Name the blood parasite species.
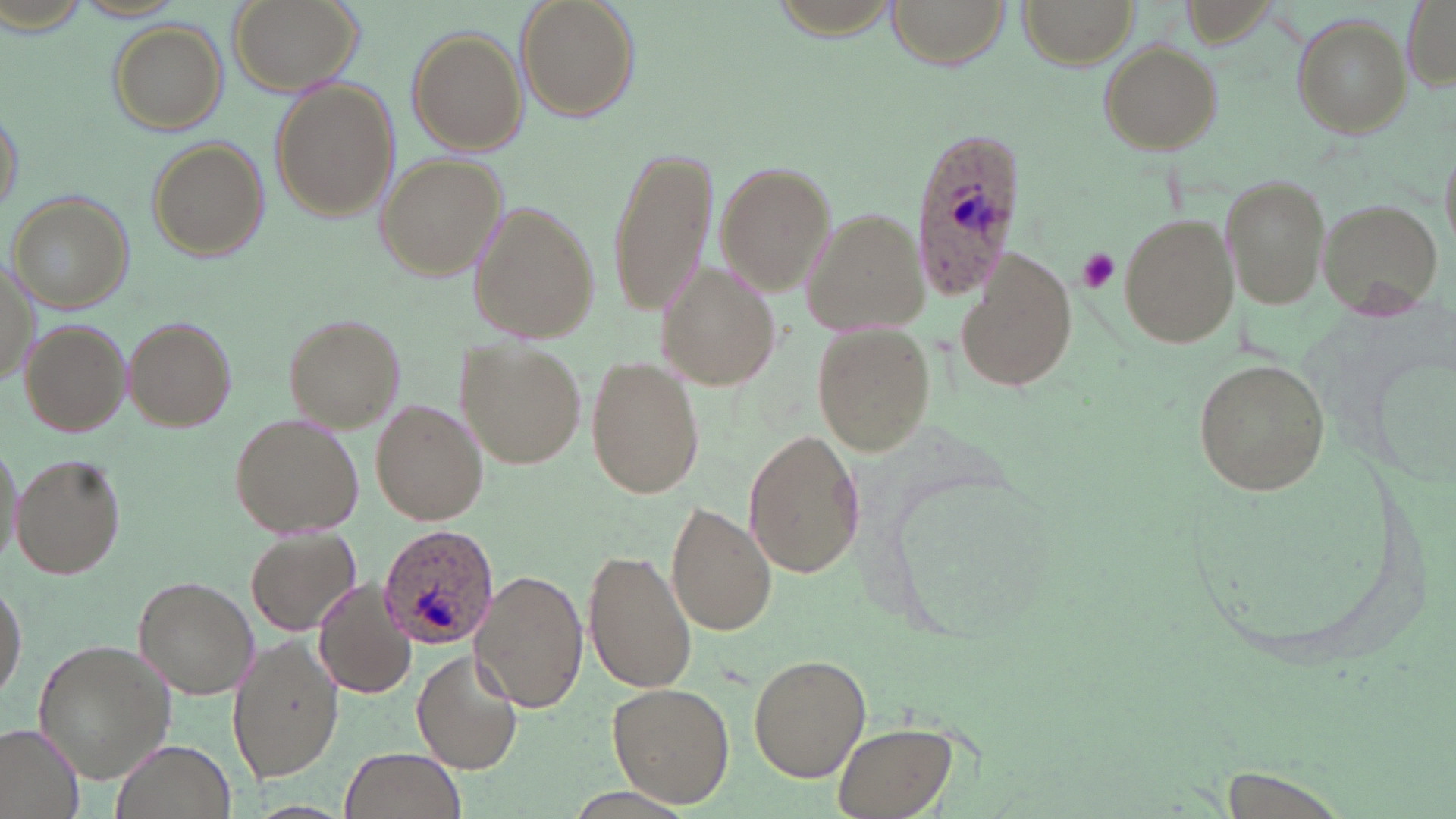
Plasmodium ovale.

Summary:
  - Coordinate format: approximate bounding boxes as (x1,y1)-(x2,y2) corner pairs in pixels
  - Platelet locations: (1075,248)-(1121,294)
  - Plasmodium ovale-infected red blood cell locations: (908,125)-(1028,299), (376,522)-(499,650)
  - Uninfected red blood cell locations: (226,0)-(368,100), (515,0)-(639,120), (884,0)-(1009,68), (1017,0)-(1136,67), (1401,0)-(1455,90), (72,2)-(190,22), (1292,13)-(1411,138), (109,23)-(228,134), (406,29)-(526,154), (1097,41)-(1223,154), (270,79)-(400,222), (1,109)-(25,215), (146,138)-(268,262), (605,144)-(720,317), (377,154)-(507,281), (713,161)-(834,292), (1221,171)-(1332,310), (6,191)-(133,314), (1314,197)-(1444,321), (468,200)-(599,342), (801,205)-(930,334), (1117,208)-(1238,349), (956,250)-(1078,394), (656,260)-(779,391), (0,261)-(36,388), (283,315)-(404,429), (124,316)-(237,430), (811,319)-(938,457), (19,320)-(131,434), (457,338)-(586,471), (1361,342)-(1456,488), (586,355)-(705,501), (1194,356)-(1331,500), (371,400)-(484,525), (229,412)-(364,539), (743,428)-(865,580), (1,435)-(21,571), (12,454)-(125,578), (886,474)-(1067,647), (665,502)-(776,636), (245,528)-(360,636), (584,547)-(698,695), (470,569)-(588,713), (132,576)-(257,698), (0,579)-(26,701), (313,579)-(417,700), (227,632)-(344,783), (31,638)-(177,782), (412,648)-(523,773), (748,654)-(871,782), (608,681)-(733,808), (831,721)-(964,819), (0,722)-(84,819), (110,739)-(235,819), (338,747)-(466,819), (1216,770)-(1357,819)
  - Stain: May-Grünwald-Giemsa
  - Image size: 1456×819 pixels
  - Modality: optical microscopy
  - Field of view: one of a larger specimen
  - Magnification: 1000x
  - Preparation: thin blood smear